Assess this cell for malaria.
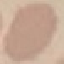

Uninfected.

Summary:
  - Image type: cell patch, automatically extracted from a larger field of view and resized to 64 × 64 pixels
  - Capture: smartphone through the microscope eyepiece
  - Stain: Giemsa
  - Preparation: thin smear